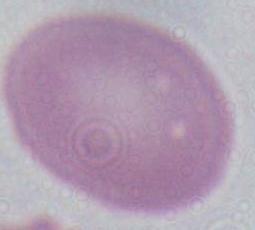

Summary:
  - Magnification: 1000x
  - Identification: erythrocyte
  - Modality: photomicrograph